Identify the preparation type.
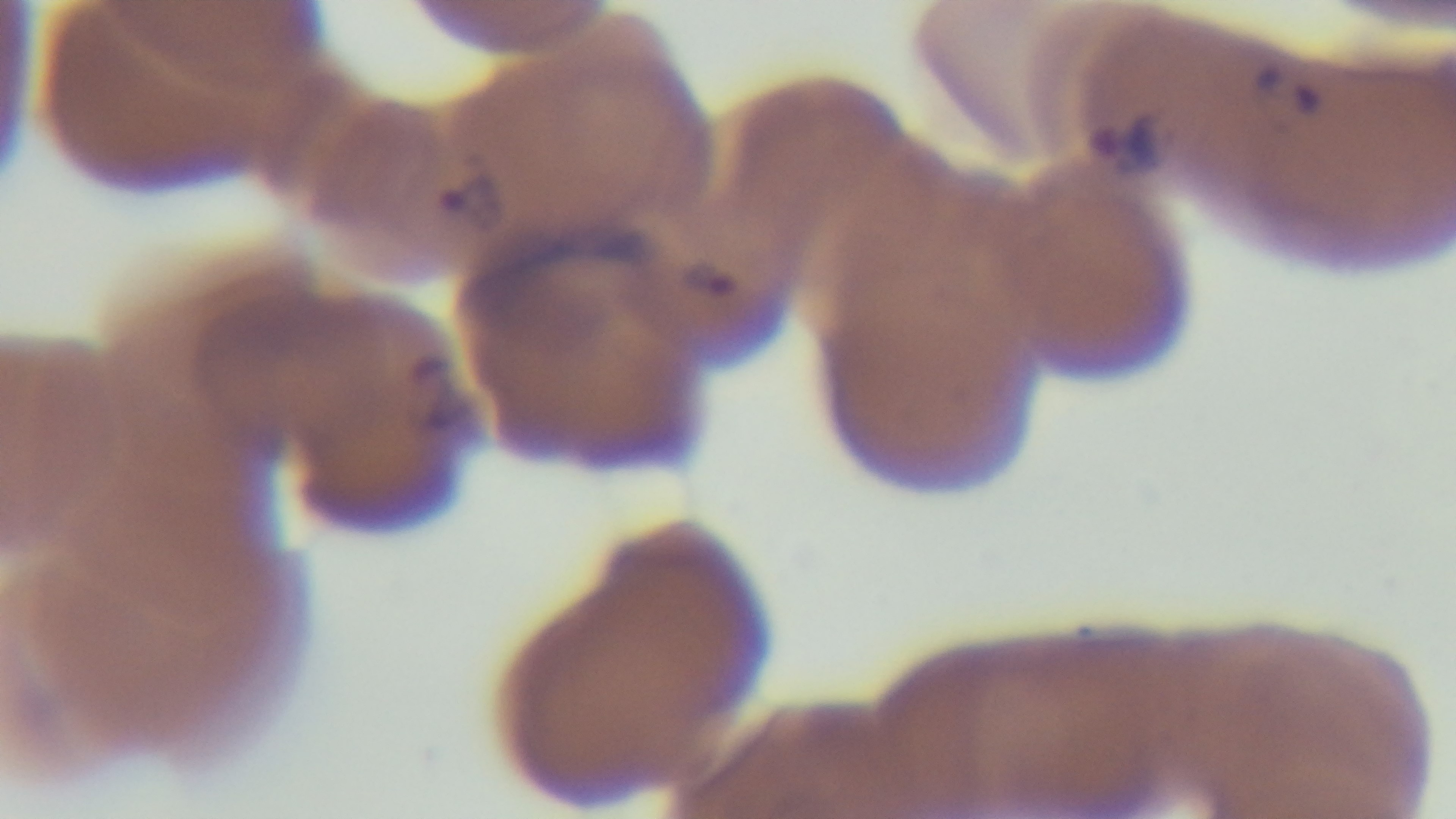
A thin smear.

One field from the slide. Mounted 4K digital camera. Malaria status: infected. Giemsa-stained. Light microscopy. Oil-immersion objective, 100x.